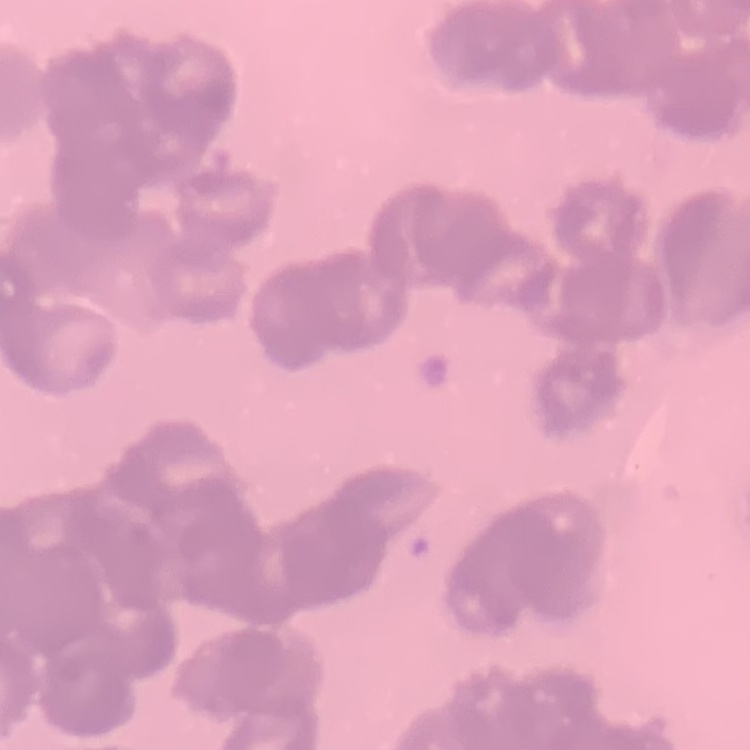

Summary:
  - Red blood cell morphology: rouleaux formation
  - Image type: one tile cut from a larger photomicrograph
  - Stain: Field's or Giemsa
  - Preparation: thin peripheral smear